Give the preparation type.
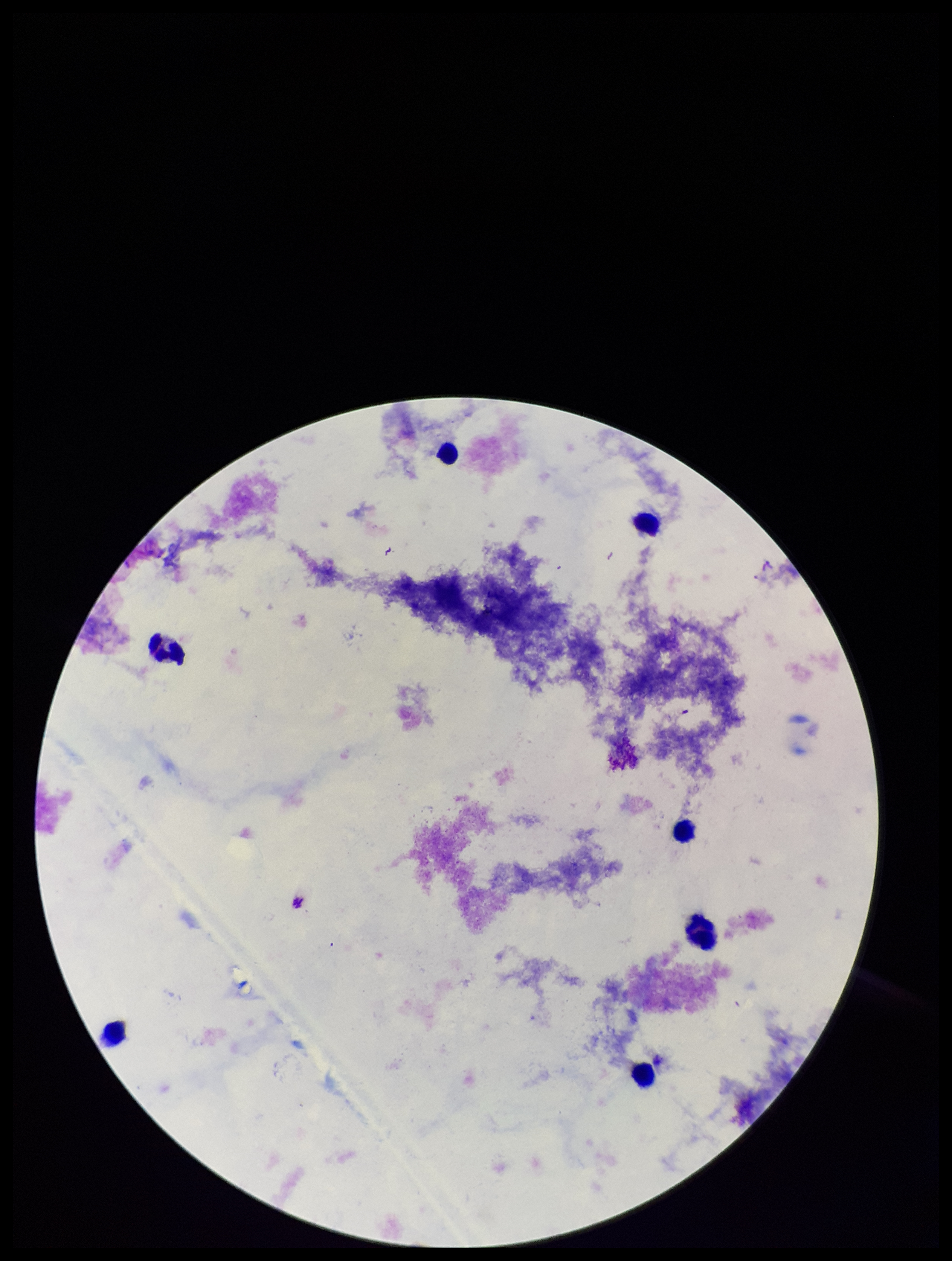

A thick smear.

Summary:
  - Image size: 952×1261 pixels
  - Parasite count: 0
  - Field of view: one from this slide
  - Leukocyte count: 7
  - Capture: smartphone photograph through the microscope eyepiece
  - Plasmodium parasites: none detected
  - Stain: Giemsa
  - Patient malaria status: negative